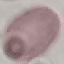

malaria_status: uninfected
capture: smartphone through the microscope eyepiece
stain: Giemsa
image_type: automatically extracted cell patch, resized to 64 × 64 pixels
preparation: thin blood smear